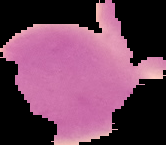
Malaria status: uninfected. The area outside the segmented cell region is set to black. Image is 166×145 pixels. From a thin blood smear.